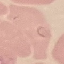
malaria_status: parasitized
image_type: cell patch, automatically extracted from a larger field of view and resized to 64 × 64 pixels
preparation: thin blood film
stain: Giemsa
capture: smartphone through the microscope eyepiece